Report the malaria status of this cell.
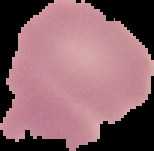

It is uninfected.

image type = cell region segmented out of the field of view; surrounding area masked to black
preparation = thin blood smear
image size = 154×151 pixels